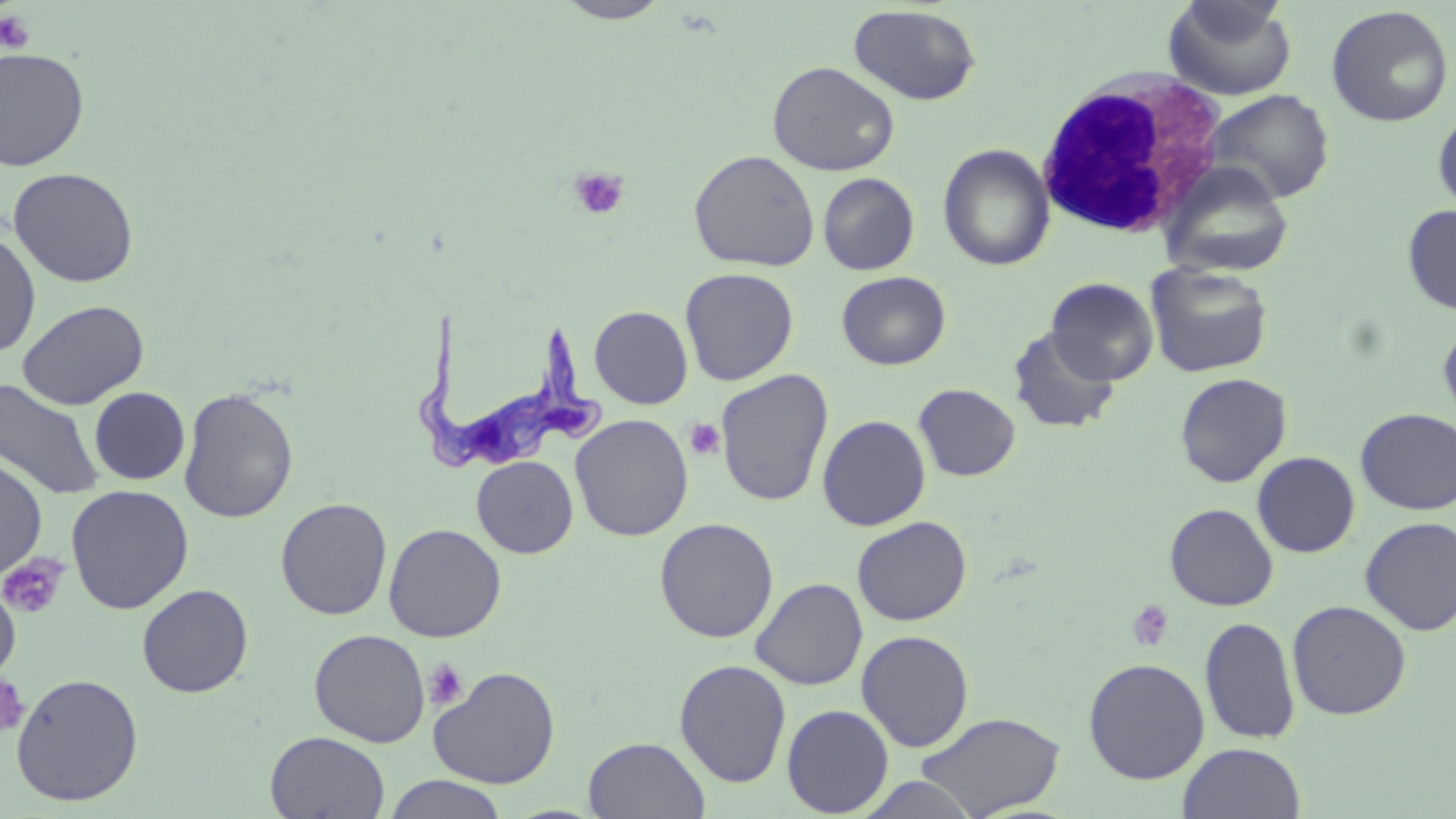
slide-level diagnosis = Trypanosoma brucei
stain = May-Grünwald-Giemsa
uninfected red blood cell locations = approximate bounding boxes as [x1, y1, x2, y2] in pixels: [554, 0, 671, 23], [1163, 0, 1298, 101], [847, 4, 982, 106], [1325, 4, 1454, 127], [0, 46, 90, 171], [767, 61, 900, 176], [1203, 88, 1335, 205], [1433, 107, 1456, 217], [937, 143, 1055, 271], [688, 149, 820, 271], [1159, 161, 1295, 280], [7, 167, 139, 288], [817, 172, 920, 275], [1402, 204, 1456, 315], [0, 229, 41, 359], [1145, 262, 1273, 378], [679, 267, 799, 386], [836, 271, 951, 370], [1046, 277, 1159, 384], [17, 299, 149, 410], [589, 306, 693, 409], [1438, 316, 1456, 427], [1009, 326, 1121, 434], [716, 369, 834, 507], [1174, 373, 1292, 487], [0, 378, 106, 501], [914, 384, 1021, 481], [89, 387, 190, 485], [178, 387, 299, 523], [1355, 408, 1456, 514], [570, 414, 694, 541], [817, 414, 931, 531], [1252, 451, 1360, 558], [0, 455, 48, 580], [472, 456, 578, 558], [65, 484, 194, 614], [275, 497, 393, 620], [1165, 503, 1278, 611], [275, 512, 504, 628], [852, 516, 972, 626], [654, 517, 779, 643], [1359, 517, 1456, 636], [383, 523, 507, 643], [0, 576, 21, 682], [750, 577, 868, 690], [137, 584, 253, 698], [1287, 599, 1412, 720], [1199, 615, 1300, 745], [309, 629, 430, 747], [856, 630, 974, 752], [1083, 657, 1210, 784], [674, 658, 792, 788], [428, 665, 561, 789], [10, 672, 144, 806], [782, 704, 894, 817], [916, 711, 1066, 818], [265, 731, 390, 818], [583, 736, 710, 818], [1178, 742, 1306, 819], [381, 774, 509, 818], [855, 774, 982, 817]
platelet locations = approximate bounding boxes as [x1, y1, x2, y2] in pixels: [0, 10, 35, 54], [568, 167, 629, 221], [685, 418, 725, 461], [1, 553, 70, 619], [1127, 599, 1175, 652], [424, 658, 469, 711], [0, 675, 29, 738]
magnification = 1000x
field of view = one of a larger specimen
image size = 1456×819 pixels
white blood cell locations = approximate bounding boxes as [x1, y1, x2, y2] in pixels: [1034, 69, 1230, 239]
preparation = thin blood smear
Trypanosoma brucei locations = approximate bounding boxes as [x1, y1, x2, y2] in pixels: [413, 309, 602, 474]
modality = light microscopy